State which parasite is depicted.
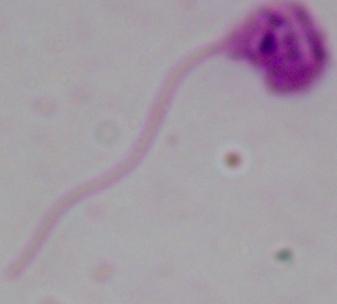

Leishmania.

Summary:
  - Modality: photomicrograph
  - Magnification: 1000x